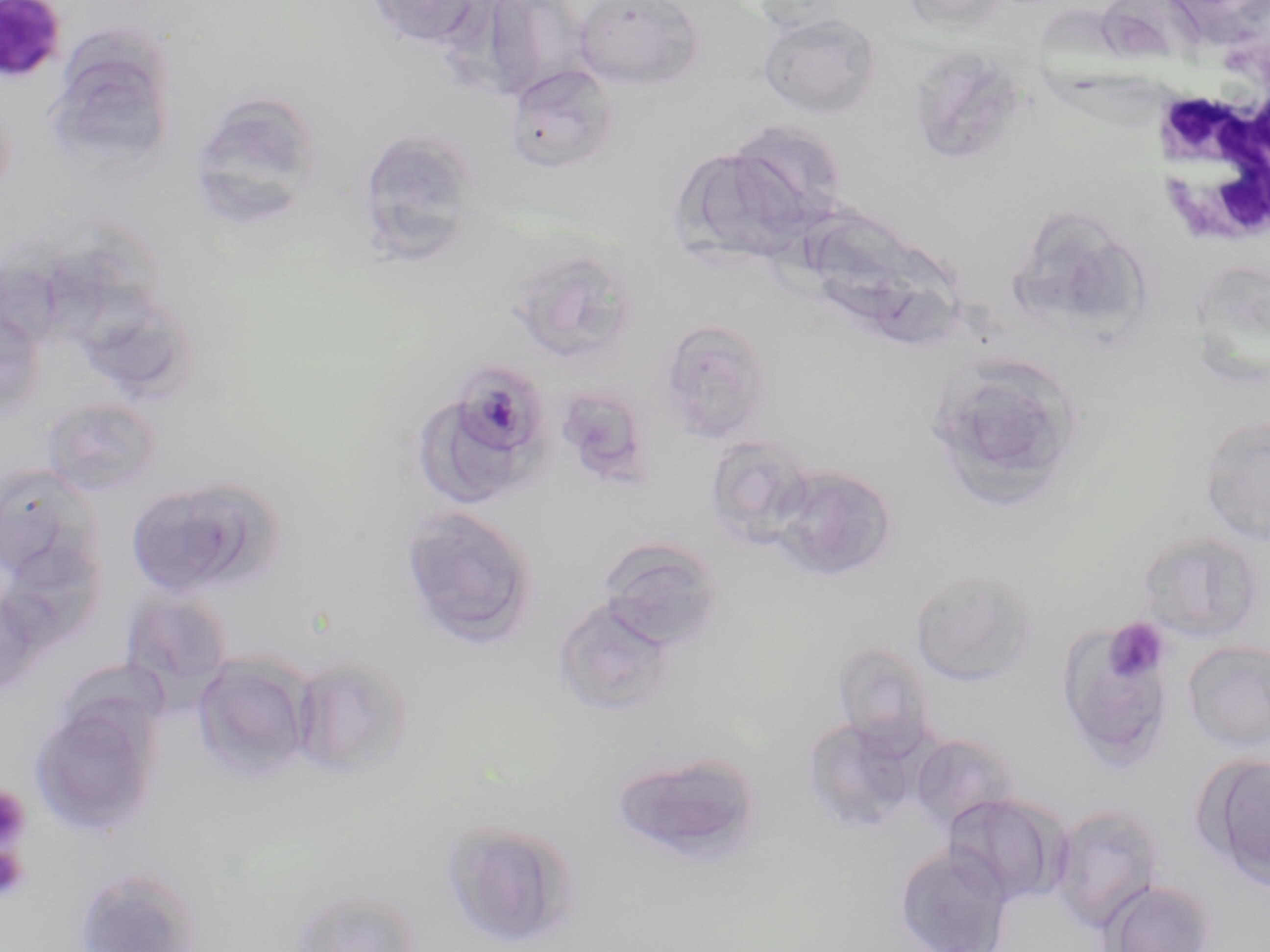
Summary:
  - Coordinate format: approximate bounding boxes as (x1, y1, x2, y2) in pixels
  - White blood cell locations: (1147, 73, 1269, 257)
  - Uninfected red blood cell locations: (364, 0, 488, 50), (574, 0, 704, 89), (902, 0, 1011, 32), (482, 1, 592, 101), (758, 12, 881, 118), (918, 38, 1022, 163), (505, 64, 619, 172), (59, 66, 171, 180), (189, 93, 321, 222), (698, 123, 847, 249), (355, 127, 482, 264), (812, 212, 930, 329), (1039, 221, 1154, 356), (39, 234, 166, 360), (506, 247, 638, 364), (1191, 270, 1270, 388), (86, 295, 199, 396), (0, 308, 46, 421), (660, 319, 772, 443), (924, 353, 1086, 514), (556, 393, 650, 491), (41, 395, 162, 497), (418, 399, 523, 504), (1199, 413, 1270, 545), (704, 434, 814, 545), (0, 463, 103, 578), (769, 465, 897, 582), (125, 475, 281, 599), (400, 504, 539, 649), (1135, 528, 1267, 643), (597, 536, 726, 651), (1, 540, 106, 650), (909, 569, 1040, 688), (120, 587, 235, 694), (554, 597, 676, 719), (1056, 618, 1177, 765), (1183, 640, 1270, 751), (831, 641, 934, 750), (192, 654, 314, 783), (50, 656, 170, 746), (291, 656, 415, 782), (29, 698, 161, 835), (802, 716, 922, 831), (909, 733, 1021, 834), (610, 750, 763, 870), (1197, 752, 1270, 888), (942, 793, 1070, 907), (1049, 803, 1166, 933), (441, 819, 579, 946), (894, 846, 1014, 952), (71, 864, 205, 952), (1102, 879, 1217, 952), (288, 886, 423, 952)
  - Plasmodium malariae-infected red blood cell locations: (0, 0, 68, 83), (454, 361, 549, 461)
  - Platelet locations: (1104, 617, 1171, 684), (0, 785, 32, 850), (0, 845, 29, 902)
  - Slide-level diagnosis: Plasmodium malariae
  - Image size: 1270×952 pixels
  - Preparation: thin blood smear
  - Stain: May-Grünwald-Giemsa
  - Modality: optical microscopy
  - Field of view: one of a larger specimen
  - Magnification: 1000x